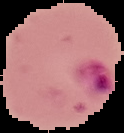
Cell region segmented out of the field of view; the surrounding area is masked to black. Image is 124×133 pixels. Malaria status: parasitized. From a thin blood film.